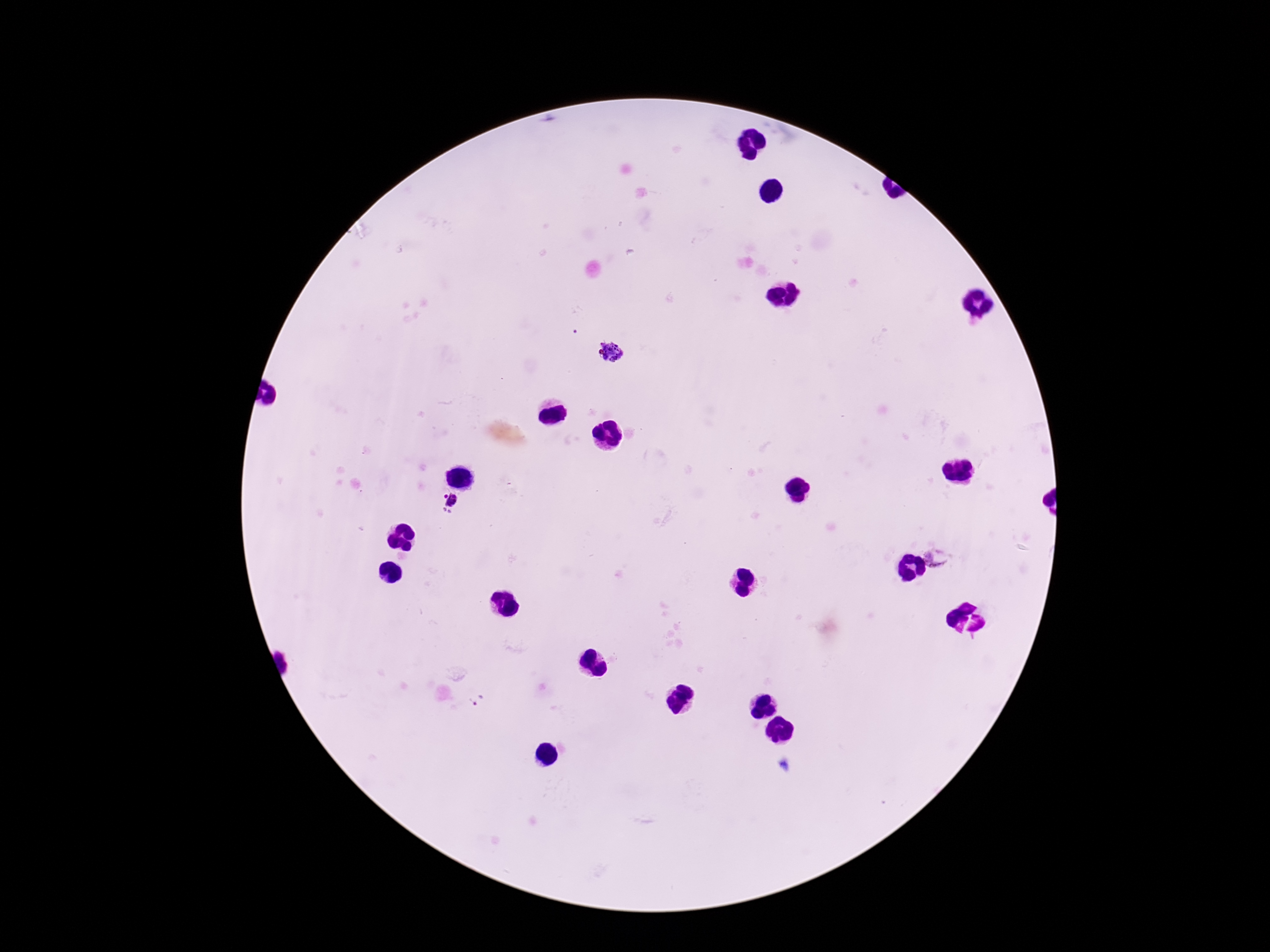
Approximate object centers, in pixels from the top-left corner. Plasmodium parasite locations: (x=609, y=351), (x=449, y=504), (x=939, y=555), (x=477, y=700). Image is 1270×952 pixels. Patient malaria status: infected. Photographed through the microscope eyepiece with a smartphone camera. Thick blood smear. One field from this slide. 100x magnification. Giemsa stain.